Locate platelets.
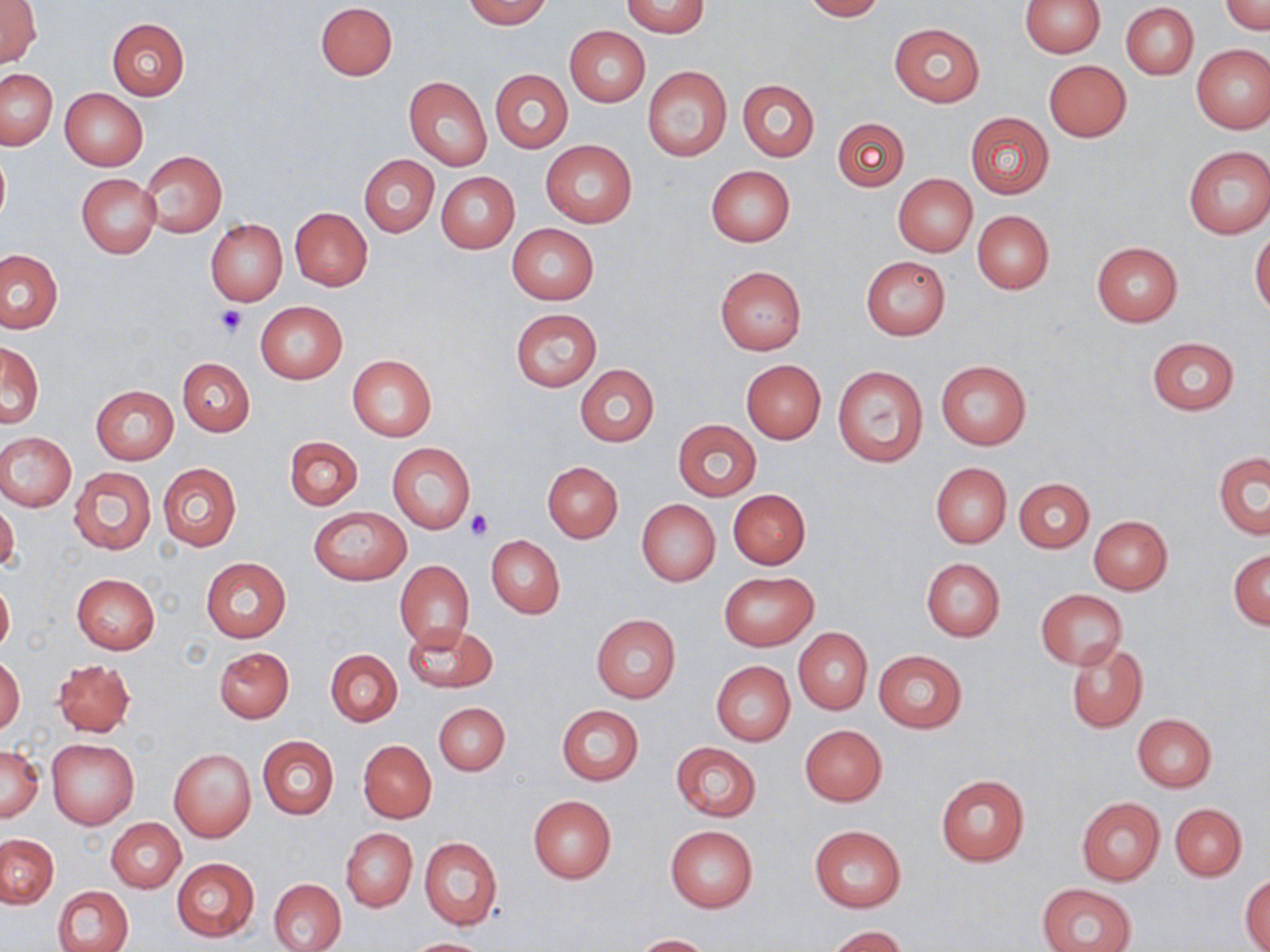

Approximate bounding boxes as (x1, y1, x2, y2) in pixels.
Platelets: (215, 305, 248, 337), (465, 510, 494, 541).

slide-level diagnosis = negative for blood parasites
field of view = single
magnification = 1000x
stain = May-Grünwald-Giemsa
modality = optical microscopy
image size = 1270×952 pixels
preparation = thin blood smear
uninfected red blood cell locations = approximate bounding boxes as (x1, y1, x2, y2) in pixels: (0, 0, 42, 69), (462, 0, 553, 28), (801, 0, 886, 21), (1019, 0, 1105, 58), (1222, 0, 1269, 35), (621, 1, 709, 37), (315, 2, 398, 80), (1121, 3, 1198, 80), (106, 18, 190, 100), (888, 22, 984, 105), (564, 26, 649, 107), (1191, 44, 1270, 133), (1043, 59, 1132, 141), (641, 66, 731, 162), (0, 69, 57, 149), (491, 69, 573, 154), (404, 77, 492, 171), (738, 80, 820, 161), (60, 88, 148, 171), (965, 111, 1055, 199), (833, 117, 909, 191), (541, 140, 637, 228), (0, 146, 10, 232), (1183, 146, 1270, 238), (140, 151, 227, 236), (359, 154, 439, 236), (707, 165, 794, 246), (437, 171, 519, 253), (76, 173, 160, 258), (892, 174, 977, 257), (290, 208, 372, 290), (972, 210, 1054, 293), (206, 218, 287, 306), (507, 224, 598, 305), (1250, 232, 1270, 315), (1091, 241, 1183, 326), (1, 248, 64, 334), (860, 255, 951, 340), (715, 266, 807, 355), (255, 301, 347, 385), (510, 309, 602, 390), (1146, 337, 1240, 415), (1, 343, 44, 428), (347, 355, 437, 440), (176, 357, 255, 437), (741, 360, 825, 443), (936, 361, 1031, 449), (574, 364, 658, 447), (833, 366, 928, 466), (91, 385, 178, 464), (672, 419, 761, 501), (0, 433, 76, 510), (284, 437, 362, 509), (387, 442, 475, 533), (1213, 452, 1269, 540), (158, 462, 241, 551), (543, 462, 622, 543), (931, 463, 1012, 548), (68, 467, 155, 554), (1014, 478, 1094, 552), (728, 489, 810, 569), (0, 500, 19, 575), (636, 500, 720, 585), (308, 506, 411, 584), (1089, 515, 1173, 594), (486, 535, 565, 618), (1228, 549, 1270, 630), (200, 557, 291, 642), (921, 558, 1005, 641), (394, 560, 473, 648), (718, 571, 818, 649), (71, 573, 160, 654), (0, 577, 14, 659), (1036, 589, 1126, 669), (591, 614, 681, 703), (403, 624, 497, 693), (793, 628, 872, 714), (1065, 642, 1148, 733), (214, 647, 294, 723), (326, 649, 402, 726), (873, 650, 967, 733), (0, 655, 25, 736), (53, 659, 135, 738), (712, 662, 795, 745), (434, 701, 510, 776), (558, 704, 643, 785), (1132, 714, 1217, 791), (799, 724, 887, 805), (257, 735, 339, 819), (47, 739, 139, 828), (359, 740, 436, 822), (671, 743, 761, 821), (0, 744, 43, 822), (168, 748, 257, 843), (936, 775, 1030, 866), (528, 796, 616, 883), (1076, 797, 1164, 886), (1170, 803, 1247, 880), (108, 818, 185, 892), (665, 825, 759, 912), (810, 825, 906, 911), (341, 828, 417, 910), (1, 834, 58, 908), (419, 837, 503, 931), (172, 858, 259, 941), (1241, 875, 1270, 952), (267, 878, 346, 952), (1036, 883, 1137, 952), (53, 885, 133, 952), (825, 926, 908, 952), (633, 934, 714, 952), (402, 937, 493, 952)